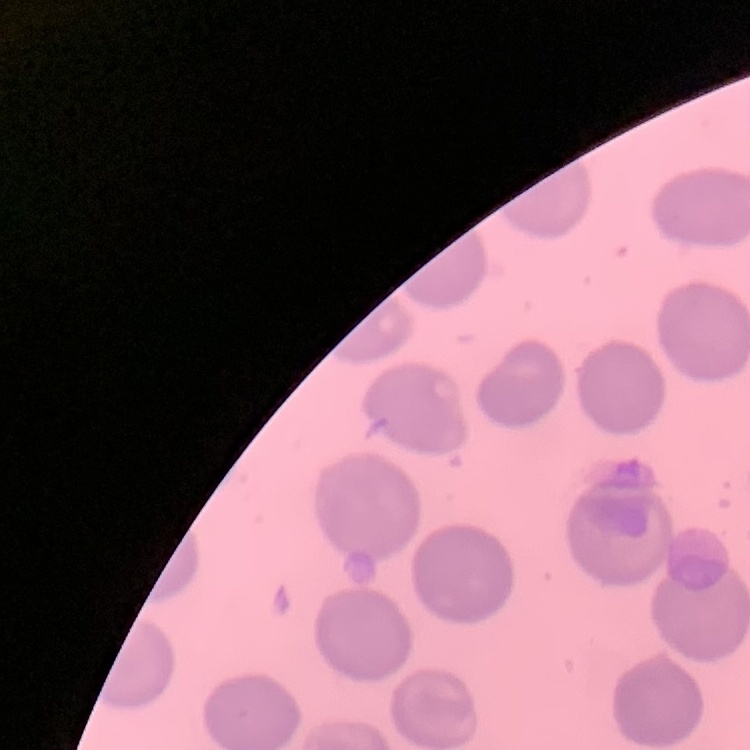

Summary:
  - Erythrocyte morphology: no rouleaux formation
  - Image type: one tile cut from a larger photomicrograph
  - Stain: Field's or Giemsa
  - Preparation: thin blood smear